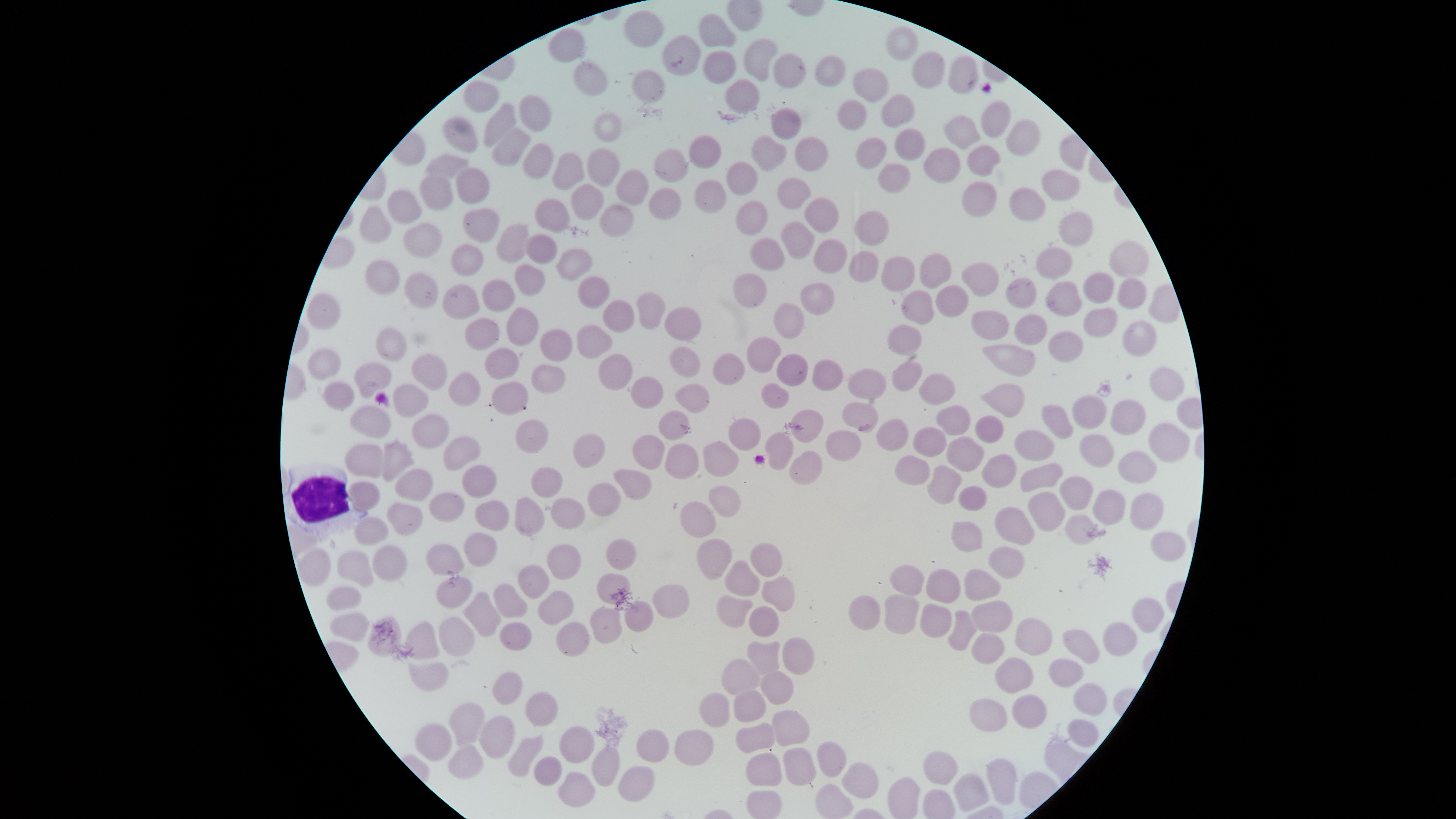 Approximate bounding boxes, in pixels from the top-left corner. Uninfected RBCs: (left=623, top=11, right=664, bottom=49), (left=698, top=14, right=736, bottom=47), (left=885, top=26, right=918, bottom=61), (left=548, top=29, right=585, bottom=63), (left=662, top=34, right=701, bottom=77), (left=743, top=38, right=777, bottom=81), (left=702, top=50, right=735, bottom=84), (left=912, top=51, right=945, bottom=89), (left=773, top=52, right=805, bottom=88), (left=815, top=54, right=846, bottom=88), (left=948, top=56, right=978, bottom=94), (left=573, top=63, right=608, bottom=97), (left=852, top=68, right=888, bottom=103), (left=632, top=70, right=666, bottom=104), (left=725, top=78, right=760, bottom=113), (left=464, top=80, right=500, bottom=113), (left=881, top=93, right=916, bottom=128), (left=518, top=96, right=551, bottom=133), (left=837, top=100, right=868, bottom=130), (left=980, top=100, right=1011, bottom=138), (left=483, top=103, right=516, bottom=148), (left=770, top=108, right=800, bottom=140), (left=593, top=113, right=622, bottom=143), (left=943, top=115, right=980, bottom=149), (left=443, top=116, right=478, bottom=153), (left=1006, top=119, right=1041, bottom=156), (left=895, top=128, right=926, bottom=161), (left=493, top=129, right=531, bottom=165), (left=688, top=135, right=722, bottom=169), (left=751, top=135, right=786, bottom=172), (left=794, top=136, right=828, bottom=172), (left=855, top=137, right=886, bottom=169), (left=522, top=143, right=552, bottom=180), (left=966, top=144, right=1000, bottom=177), (left=923, top=147, right=960, bottom=183), (left=653, top=148, right=688, bottom=183), (left=586, top=149, right=620, bottom=186), (left=552, top=153, right=585, bottom=191), (left=425, top=154, right=470, bottom=180), (left=726, top=161, right=758, bottom=196), (left=878, top=163, right=911, bottom=193), (left=455, top=167, right=490, bottom=205), (left=616, top=169, right=649, bottom=205), (left=1041, top=169, right=1081, bottom=202), (left=418, top=175, right=454, bottom=211), (left=776, top=177, right=812, bottom=211), (left=694, top=179, right=727, bottom=214), (left=962, top=181, right=997, bottom=217), (left=571, top=184, right=603, bottom=221), (left=1008, top=187, right=1046, bottom=221), (left=649, top=188, right=682, bottom=221), (left=386, top=189, right=421, bottom=225), (left=804, top=197, right=839, bottom=233), (left=535, top=199, right=570, bottom=233), (left=735, top=200, right=768, bottom=236), (left=599, top=204, right=634, bottom=238), (left=359, top=205, right=391, bottom=243), (left=461, top=207, right=499, bottom=243), (left=853, top=210, right=890, bottom=246), (left=1058, top=210, right=1093, bottom=247), (left=780, top=221, right=814, bottom=260), (left=401, top=222, right=443, bottom=258), (left=496, top=223, right=529, bottom=264), (left=525, top=234, right=557, bottom=265), (left=750, top=237, right=785, bottom=272), (left=814, top=240, right=847, bottom=273), (left=1108, top=240, right=1149, bottom=277), (left=451, top=245, right=484, bottom=277), (left=1035, top=247, right=1072, bottom=279), (left=555, top=248, right=593, bottom=282), (left=848, top=250, right=879, bottom=284), (left=920, top=254, right=952, bottom=288), (left=881, top=256, right=915, bottom=292), (left=364, top=259, right=400, bottom=296), (left=961, top=262, right=999, bottom=297), (left=514, top=263, right=545, bottom=297), (left=404, top=272, right=438, bottom=309), (left=1082, top=272, right=1114, bottom=304), (left=732, top=273, right=767, bottom=308), (left=577, top=275, right=610, bottom=309), (left=1005, top=277, right=1037, bottom=309), (left=1117, top=278, right=1147, bottom=310), (left=482, top=279, right=515, bottom=312), (left=1044, top=281, right=1082, bottom=316), (left=800, top=282, right=835, bottom=316), (left=442, top=284, right=479, bottom=320), (left=935, top=284, right=970, bottom=318), (left=900, top=290, right=934, bottom=326), (left=306, top=292, right=340, bottom=330), (left=635, top=292, right=665, bottom=331), (left=602, top=299, right=635, bottom=332), (left=773, top=303, right=804, bottom=340), (left=506, top=307, right=539, bottom=346), (left=664, top=307, right=701, bottom=341), (left=1082, top=307, right=1118, bottom=338), (left=970, top=311, right=1010, bottom=340), (left=1013, top=314, right=1047, bottom=345), (left=464, top=318, right=500, bottom=351), (left=1122, top=321, right=1158, bottom=357), (left=887, top=324, right=922, bottom=356), (left=577, top=325, right=612, bottom=360), (left=375, top=327, right=407, bottom=362), (left=539, top=329, right=573, bottom=362), (left=1048, top=331, right=1084, bottom=363), (left=746, top=336, right=781, bottom=373), (left=981, top=344, right=1036, bottom=377), (left=669, top=346, right=701, bottom=379), (left=484, top=347, right=520, bottom=380), (left=307, top=348, right=340, bottom=379), (left=713, top=352, right=744, bottom=387), (left=411, top=354, right=447, bottom=391), (left=598, top=354, right=633, bottom=391), (left=775, top=354, right=808, bottom=387), (left=812, top=359, right=844, bottom=391), (left=354, top=361, right=392, bottom=399), (left=891, top=361, right=923, bottom=392), (left=531, top=364, right=565, bottom=394), (left=1149, top=367, right=1185, bottom=402), (left=848, top=369, right=886, bottom=400), (left=447, top=372, right=481, bottom=407), (left=918, top=373, right=954, bottom=405), (left=630, top=377, right=664, bottom=409), (left=322, top=381, right=355, bottom=411), (left=491, top=381, right=529, bottom=416), (left=760, top=382, right=789, bottom=409), (left=675, top=383, right=710, bottom=414), (left=392, top=384, right=429, bottom=418), (left=980, top=384, right=1025, bottom=418), (left=1071, top=395, right=1107, bottom=429), (left=1110, top=399, right=1146, bottom=436), (left=841, top=402, right=879, bottom=433), (left=935, top=405, right=970, bottom=437), (left=1041, top=405, right=1073, bottom=440), (left=349, top=406, right=391, bottom=439), (left=790, top=409, right=824, bottom=443), (left=659, top=411, right=689, bottom=440), (left=412, top=414, right=449, bottom=450), (left=974, top=415, right=1003, bottom=444), (left=728, top=417, right=761, bottom=451), (left=515, top=419, right=549, bottom=454), (left=876, top=419, right=909, bottom=452), (left=1148, top=423, right=1190, bottom=462), (left=911, top=427, right=947, bottom=457), (left=825, top=430, right=860, bottom=462), (left=1014, top=430, right=1054, bottom=461), (left=765, top=432, right=794, bottom=471), (left=1078, top=433, right=1114, bottom=467), (left=572, top=434, right=606, bottom=469), (left=631, top=434, right=665, bottom=470), (left=443, top=436, right=481, bottom=472), (left=946, top=436, right=984, bottom=473), (left=381, top=439, right=415, bottom=483), (left=703, top=441, right=739, bottom=476), (left=344, top=443, right=383, bottom=479), (left=665, top=444, right=699, bottom=478), (left=789, top=451, right=823, bottom=485), (left=1118, top=451, right=1156, bottom=484), (left=982, top=454, right=1016, bottom=489), (left=894, top=455, right=930, bottom=486), (left=1021, top=462, right=1063, bottom=493), (left=461, top=464, right=497, bottom=499), (left=927, top=465, right=962, bottom=505), (left=531, top=467, right=562, bottom=499), (left=394, top=468, right=433, bottom=501), (left=613, top=469, right=651, bottom=501), (left=1059, top=476, right=1093, bottom=511), (left=349, top=481, right=380, bottom=511), (left=587, top=482, right=622, bottom=517), (left=708, top=486, right=741, bottom=518), (left=958, top=486, right=987, bottom=512), (left=1092, top=490, right=1127, bottom=526), (left=1027, top=491, right=1066, bottom=532), (left=428, top=492, right=465, bottom=523), (left=1129, top=493, right=1164, bottom=530), (left=514, top=497, right=545, bottom=537), (left=550, top=498, right=586, bottom=529), (left=474, top=500, right=509, bottom=532), (left=679, top=501, right=716, bottom=537), (left=387, top=503, right=423, bottom=536), (left=994, top=507, right=1035, bottom=545), (left=1065, top=514, right=1099, bottom=545), (left=354, top=517, right=389, bottom=546), (left=951, top=521, right=982, bottom=552), (left=1150, top=531, right=1186, bottom=562), (left=463, top=532, right=497, bottom=568), (left=605, top=538, right=637, bottom=570), (left=696, top=538, right=732, bottom=579), (left=749, top=543, right=782, bottom=577), (left=370, top=544, right=408, bottom=581), (left=425, top=544, right=464, bottom=576), (left=547, top=544, right=581, bottom=581), (left=988, top=546, right=1025, bottom=578), (left=299, top=548, right=331, bottom=587), (left=337, top=550, right=373, bottom=586), (left=725, top=560, right=760, bottom=596), (left=517, top=565, right=549, bottom=599), (left=889, top=565, right=925, bottom=597), (left=926, top=568, right=962, bottom=604), (left=964, top=569, right=1002, bottom=601), (left=597, top=574, right=630, bottom=605), (left=762, top=576, right=795, bottom=611), (left=435, top=577, right=474, bottom=609), (left=493, top=583, right=528, bottom=619), (left=652, top=584, right=690, bottom=620), (left=325, top=586, right=361, bottom=612), (left=537, top=590, right=574, bottom=625), (left=463, top=591, right=501, bottom=637), (left=716, top=594, right=753, bottom=628), (left=884, top=594, right=919, bottom=634), (left=848, top=595, right=880, bottom=630), (left=1131, top=597, right=1164, bottom=633), (left=971, top=600, right=1013, bottom=634), (left=624, top=601, right=654, bottom=633), (left=919, top=603, right=953, bottom=638), (left=748, top=606, right=780, bottom=637), (left=589, top=608, right=622, bottom=645), (left=948, top=610, right=977, bottom=651), (left=329, top=612, right=369, bottom=642), (left=368, top=616, right=401, bottom=657), (left=439, top=617, right=475, bottom=657), (left=1014, top=618, right=1053, bottom=656), (left=405, top=622, right=440, bottom=660), (left=499, top=622, right=531, bottom=651), (left=556, top=622, right=589, bottom=657), (left=1102, top=622, right=1137, bottom=656), (left=1062, top=629, right=1100, bottom=664), (left=971, top=633, right=1004, bottom=665), (left=782, top=636, right=815, bottom=676), (left=746, top=641, right=781, bottom=675), (left=994, top=657, right=1034, bottom=694), (left=720, top=658, right=760, bottom=695), (left=1048, top=659, right=1084, bottom=688), (left=407, top=662, right=449, bottom=692), (left=492, top=671, right=522, bottom=705), (left=760, top=671, right=793, bottom=705), (left=1073, top=683, right=1107, bottom=716), (left=732, top=690, right=766, bottom=722), (left=525, top=692, right=558, bottom=727), (left=699, top=692, right=730, bottom=727), (left=1011, top=694, right=1047, bottom=729), (left=969, top=699, right=1008, bottom=732), (left=448, top=702, right=485, bottom=746), (left=770, top=710, right=810, bottom=746), (left=479, top=715, right=515, bottom=758), (left=1067, top=718, right=1098, bottom=748), (left=415, top=722, right=453, bottom=762), (left=734, top=722, right=775, bottom=754), (left=559, top=725, right=595, bottom=763), (left=636, top=728, right=670, bottom=763), (left=674, top=729, right=714, bottom=767), (left=508, top=735, right=543, bottom=777), (left=816, top=742, right=847, bottom=778), (left=447, top=745, right=484, bottom=780), (left=591, top=745, right=621, bottom=786), (left=783, top=747, right=817, bottom=785), (left=923, top=751, right=958, bottom=785), (left=746, top=753, right=782, bottom=786), (left=533, top=756, right=562, bottom=786), (left=986, top=758, right=1017, bottom=805), (left=842, top=762, right=880, bottom=800), (left=618, top=765, right=655, bottom=803), (left=558, top=772, right=595, bottom=806), (left=953, top=773, right=989, bottom=812). WBCs: (left=283, top=461, right=368, bottom=541). Photographed with a smartphone camera through the microscope eyepiece. Single field of view. Giemsa-stained preparation. Presence: no malaria parasites detected. Image is 1456×819 pixels. The visible region is circular. Thin blood smear.